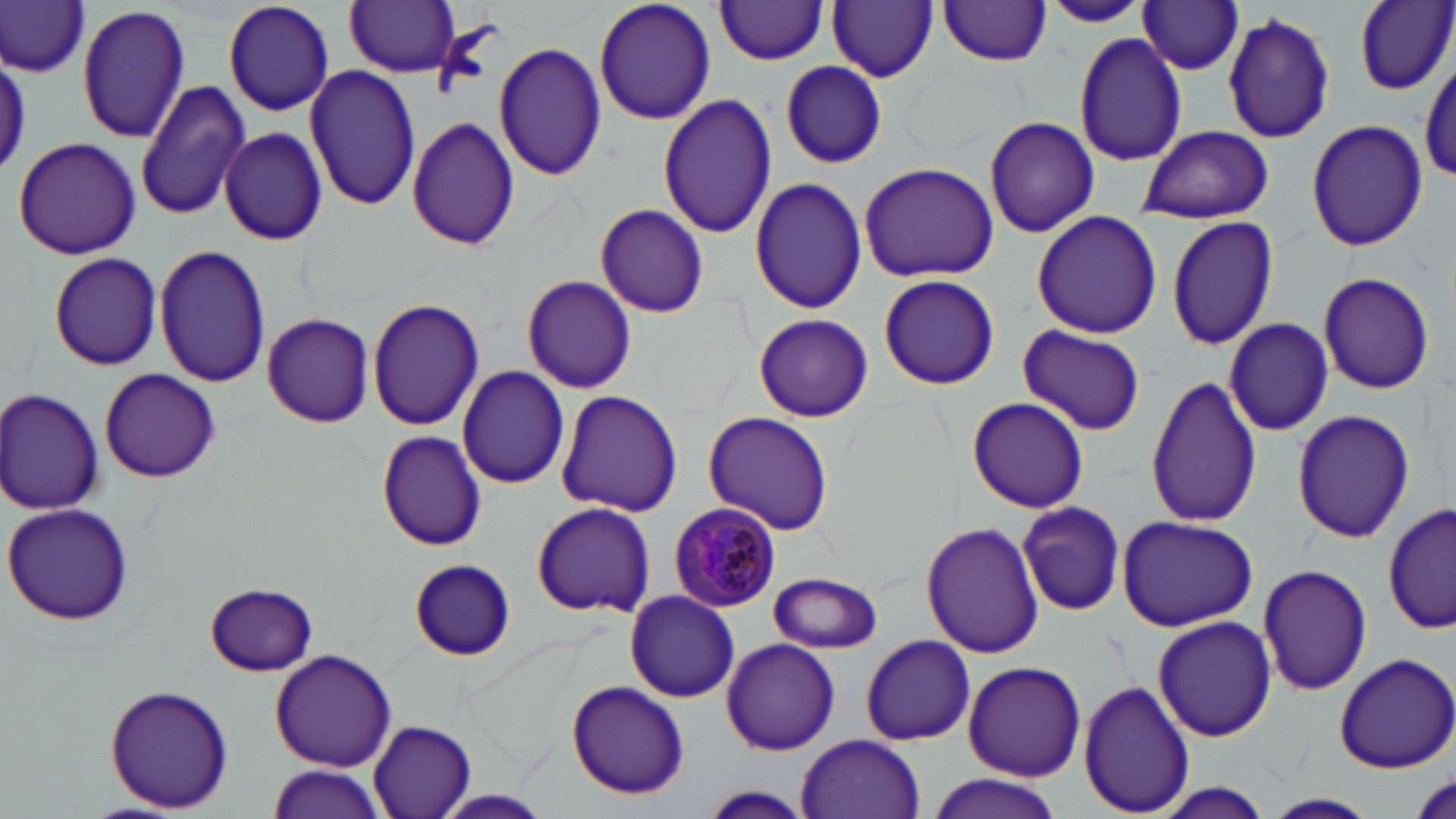

Summary:
  - Coordinate format: approximate bounding boxes as (x1,y1)-(x2,y2) corner pairs in pixels
  - Uninfected red blood cell locations: (0,0)-(90,79), (223,0)-(334,117), (345,0)-(460,78), (593,0)-(717,126), (828,0)-(937,83), (1354,0)-(1455,95), (713,1)-(831,64), (936,1)-(1054,66), (1039,1)-(1153,27), (1137,2)-(1246,75), (79,6)-(189,142), (1222,11)-(1338,142), (1072,31)-(1190,168), (494,41)-(608,182), (1419,59)-(1455,189), (780,61)-(887,168), (304,63)-(422,213), (135,80)-(253,221), (657,93)-(777,239), (984,114)-(1100,240), (407,115)-(520,251), (1306,117)-(1427,252), (1138,124)-(1273,223), (218,127)-(328,246), (12,136)-(143,260), (859,161)-(999,282), (749,176)-(869,314), (594,205)-(709,318), (1031,211)-(1163,338), (1167,213)-(1280,351), (153,242)-(271,388), (48,251)-(162,372), (1316,271)-(1434,395), (877,274)-(1000,391), (520,275)-(637,394), (367,297)-(484,432), (261,312)-(374,428), (753,313)-(874,422), (1223,317)-(1335,437), (1184,321)-(1310,476), (1018,325)-(1146,435), (457,366)-(572,489), (98,368)-(221,483), (1145,373)-(1264,528), (0,388)-(105,515), (555,390)-(683,517), (966,397)-(1090,512), (1290,409)-(1416,544), (703,412)-(835,537), (375,430)-(487,550), (1383,499)-(1454,638), (2,500)-(135,627), (530,501)-(655,617), (1018,501)-(1125,616), (1117,515)-(1258,632), (920,521)-(1043,659), (409,560)-(519,661), (1257,563)-(1372,696), (769,571)-(883,652), (202,582)-(319,675), (624,591)-(739,702), (1153,615)-(1277,742), (860,634)-(975,746), (720,638)-(840,755), (269,649)-(398,771), (1331,650)-(1456,773), (962,661)-(1086,781), (1079,678)-(1195,816), (565,679)-(690,799), (103,683)-(235,813), (368,721)-(477,819), (797,734)-(925,818), (268,764)-(386,819), (923,775)-(1064,818), (1147,782)-(1279,817), (694,785)-(820,819), (428,790)-(559,819), (1266,792)-(1377,817)
  - Plasmodium malariae-infected red blood cell locations: (665,503)-(781,615)
  - Slide-level diagnosis: Plasmodium malariae
  - Image size: 1456×819 pixels
  - Magnification: 1000x
  - Modality: light microscopy
  - Preparation: thin blood smear
  - Stain: May-Grünwald-Giemsa
  - Field of view: one of a larger specimen